Assess this cell for malaria.
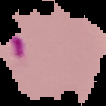

Parasitized.

From a thin blood film. Image is 106×106 pixels. Segmented cell region on a black background.